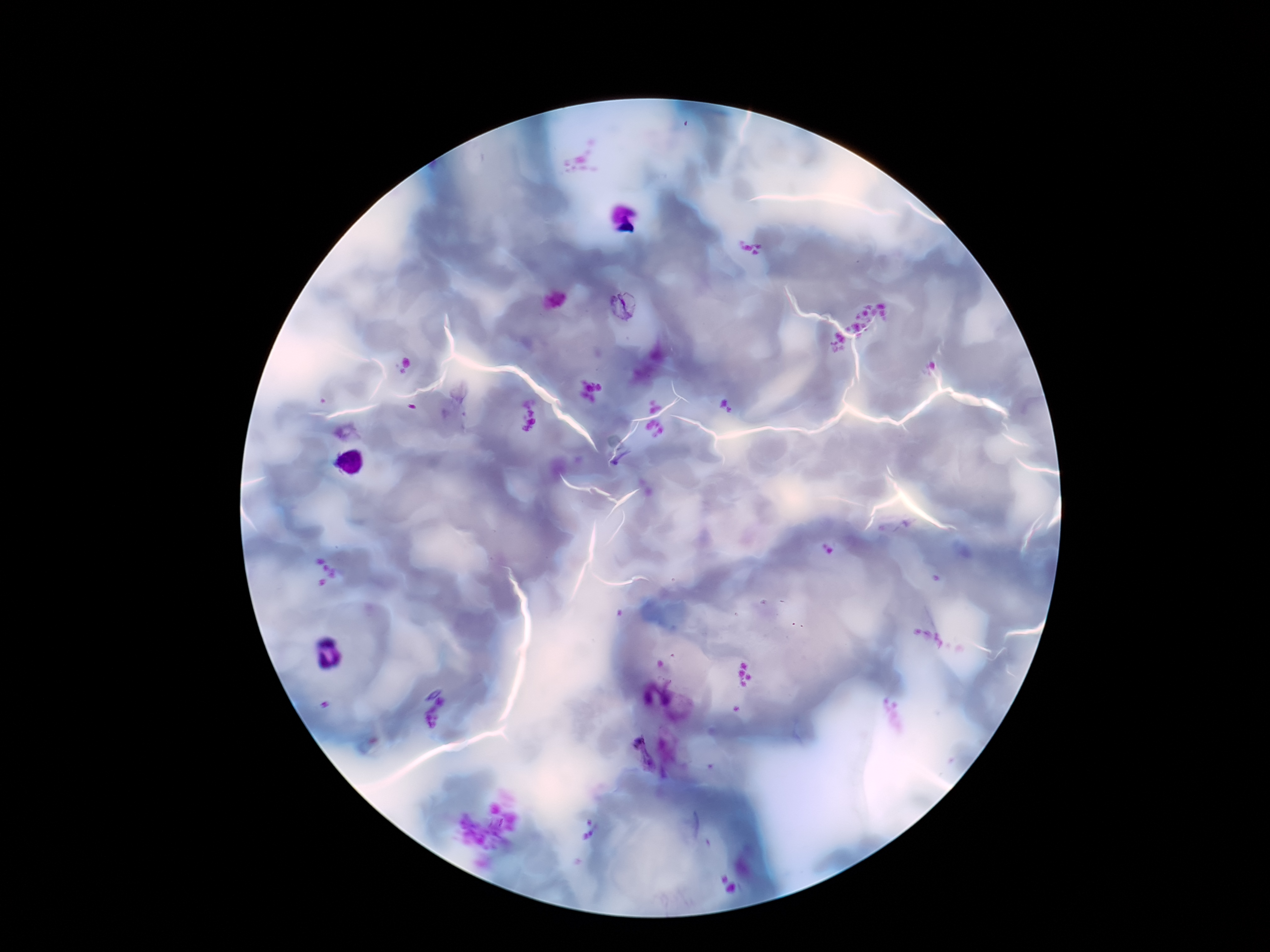
patient_malaria_status: infected
image_size: 1270×952 pixels
stain: Giemsa
magnification: 100x
field_of_view: single
preparation: thick blood smear
capture: smartphone camera through the microscope eyepiece
plasmodium_parasite_locations: 'approximate centers as {x, y} in pixels: {622, 307}, {623, 461}, {638, 755}'